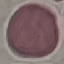
Malaria status: uninfected. Cell patch, automatically extracted from a larger field of view and resized to 64 × 64 pixels. Photographed with a smartphone camera at the microscope eyepiece. Giemsa-stained preparation. Thin blood film.